State the blood parasite species.
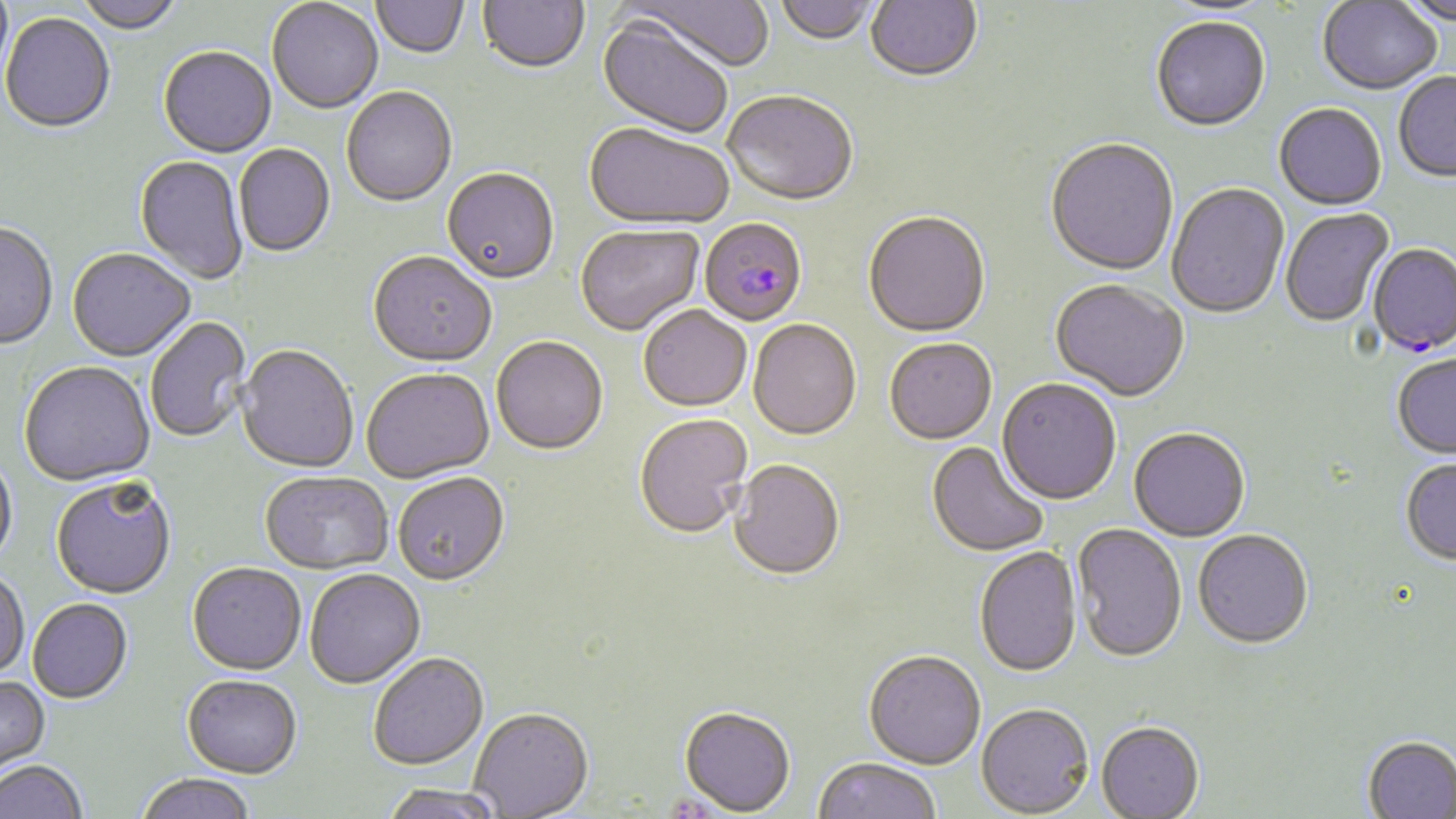
Plasmodium falciparum.

Approximate bounding boxes as [x1, y1, x2, y2] in pixels. Plasmodium falciparum-infected red blood cell locations: [700, 221, 807, 328], [1367, 245, 1456, 358]. Uninfected red blood cell locations: [74, 0, 184, 35], [372, 0, 469, 60], [478, 0, 589, 76], [623, 0, 774, 74], [865, 0, 983, 86], [1393, 0, 1456, 28], [267, 1, 384, 116], [773, 1, 879, 47], [1318, 1, 1442, 97], [1159, 3, 1276, 22], [0, 14, 115, 136], [595, 18, 733, 141], [1151, 18, 1271, 134], [158, 48, 277, 160], [1393, 73, 1456, 184], [342, 88, 458, 209], [722, 94, 858, 209], [1274, 105, 1387, 212], [584, 125, 733, 233], [1045, 140, 1178, 278], [233, 145, 336, 259], [134, 156, 248, 285], [442, 170, 559, 287], [1167, 184, 1290, 321], [1280, 209, 1395, 329], [863, 213, 990, 340], [0, 224, 58, 351], [576, 226, 705, 337], [67, 250, 195, 363], [368, 254, 497, 369], [1050, 281, 1188, 404], [639, 307, 752, 413], [146, 317, 251, 443], [748, 321, 861, 442], [491, 338, 608, 457], [884, 340, 997, 447], [237, 346, 358, 474], [1393, 354, 1456, 460], [19, 362, 155, 489], [361, 370, 494, 484], [996, 380, 1121, 507], [635, 415, 753, 540], [1129, 429, 1249, 544], [926, 442, 1050, 558], [0, 453, 18, 570], [730, 460, 844, 581], [1400, 460, 1456, 566], [259, 472, 392, 575], [393, 474, 510, 588], [51, 478, 176, 601], [1072, 524, 1187, 665], [1193, 531, 1313, 651], [974, 547, 1082, 679], [187, 564, 306, 677], [304, 570, 426, 690], [0, 571, 29, 680], [28, 600, 133, 705], [863, 651, 986, 769], [368, 654, 489, 772], [182, 676, 302, 780], [0, 678, 50, 780], [976, 703, 1093, 817], [679, 705, 796, 815], [469, 708, 594, 818], [1096, 723, 1205, 818], [1361, 737, 1456, 819], [812, 757, 941, 819], [0, 761, 87, 819], [136, 775, 257, 819], [380, 785, 505, 819]. One field of a larger specimen. 1000x magnification. Image is 1456×819 pixels. Light microscopy. Thin blood film. May-Grünwald-Giemsa-stained preparation.